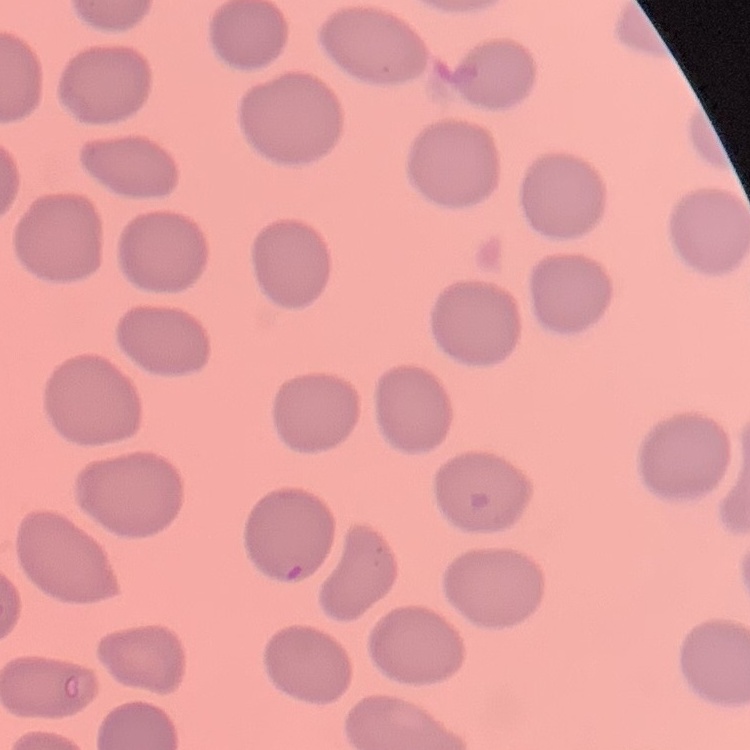 The erythrocytes exhibit no rouleaux formation. Field's or Giemsa stain. Square crop of a larger photomicrograph. Thin blood film.